Assess this cell for malaria.
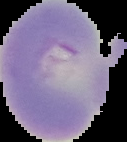

Uninfected.

Summary:
  - Image size: 127×142 pixels
  - Preparation: thin blood smear
  - Image type: segmented cell region with the area outside set to black